Locate every P. falciparum parasite and identify its life-cycle stage.
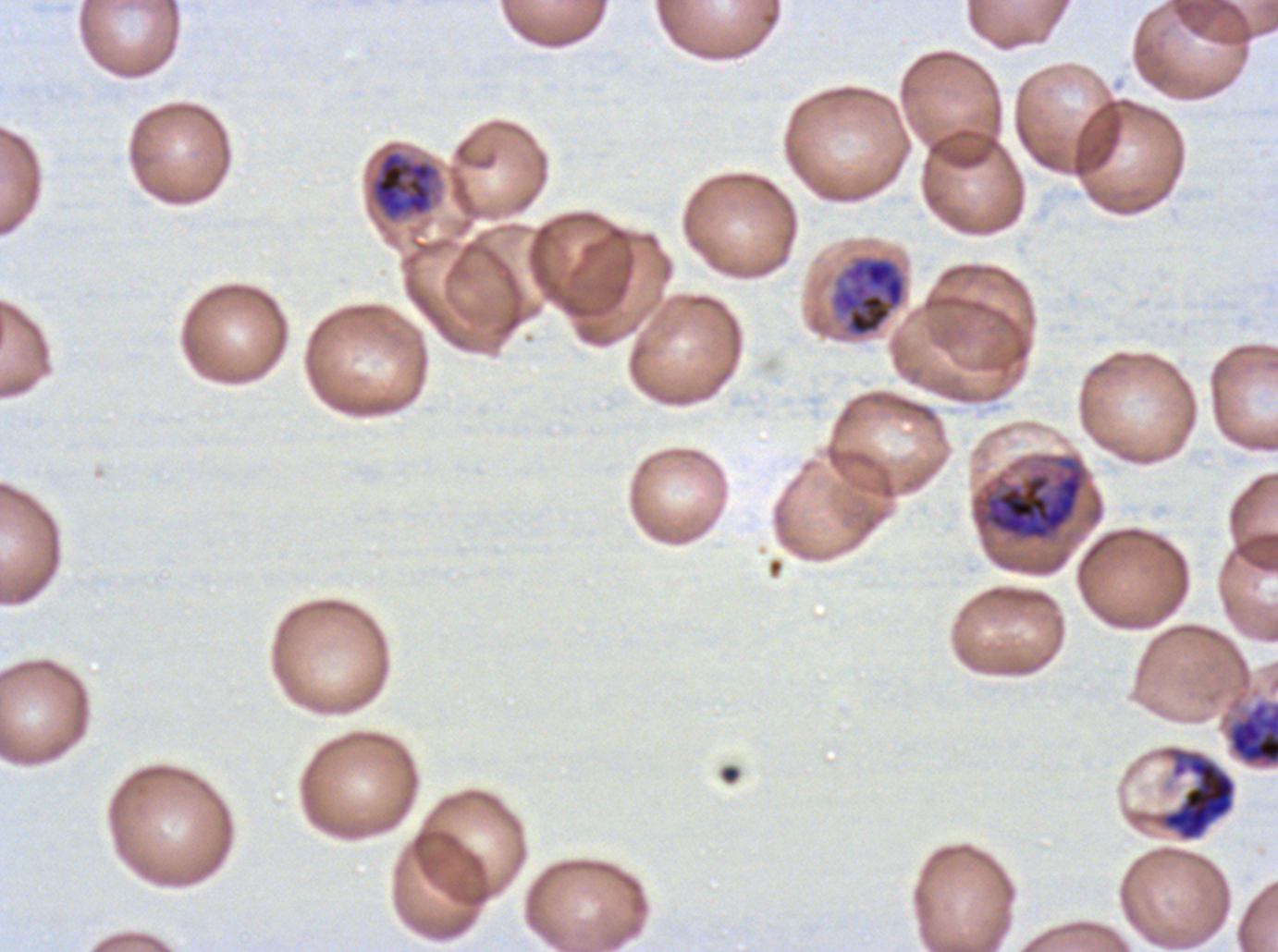
Approximate bounding rectangles given as corner coordinates in pixels from the top-left.
Late trophozoites: (x1=369, y1=150, x2=440, y2=221), (x1=829, y1=255, x2=907, y2=338).
Early schizonts: (x1=971, y1=453, x2=1089, y2=544).
Late schizonts: (x1=1227, y1=701, x2=1277, y2=768), (x1=1157, y1=746, x2=1236, y2=841).
No rings, late-ring/early-trophozoite forms, mid trophozoites, segmenters, or gametocytes observed.

debris locations = (x1=719, y1=763, x2=742, y2=786)
preparation = thin blood film
life-cycle stages observed = late trophozoite, early schizont, late schizont
image size = 1278×952 pixels
specimen = ex-vivo P. falciparum culture from a patient in The Gambia, grown for 24 to 48 hours
field of view = one sub-image of a larger composite
stain = Giemsa